Report the malaria status of this cell.
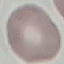
Uninfected.

Photographed with a smartphone camera at the microscope eyepiece. Thin blood smear. Giemsa-stained preparation. Cell patch, automatically extracted from a larger field of view and resized to 64 × 64 pixels.